Locate every malaria parasite.
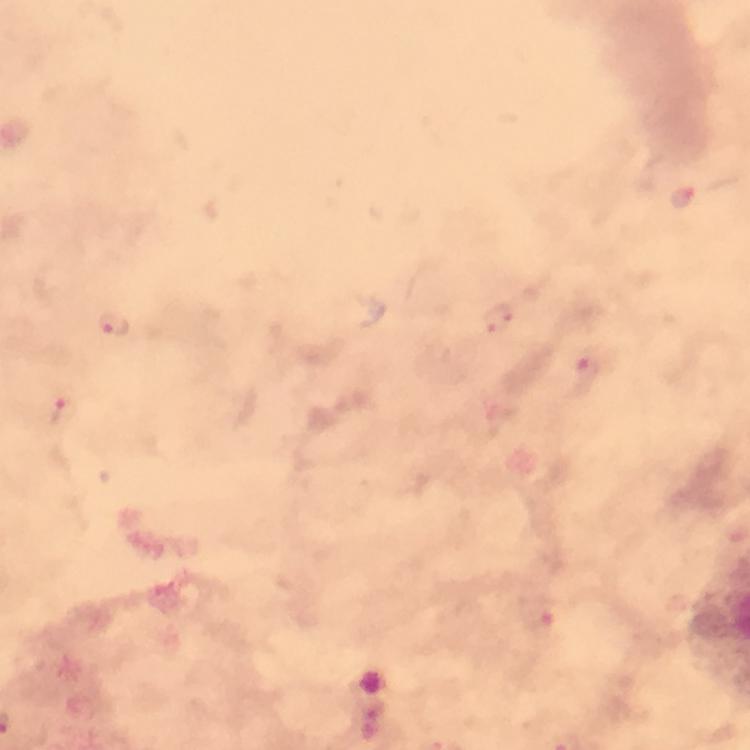
Approximate object centers, in pixels from the top-left corner.
Malaria parasites: (x=499, y=317), (x=115, y=324), (x=587, y=371), (x=65, y=410), (x=538, y=617).

Summary:
  - Cropped from: one field of view
  - Capture: smartphone mounted on the microscope
  - Stain: Giemsa
  - Magnification: 100x
  - Preparation: thick blood smear
  - Image size: 750×750 pixels
  - Context: from a diagnostic examination for malaria
  - Immersion oil: applied